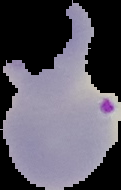

Cell region segmented out of the field of view; the surrounding area is masked to black. Result: malaria parasites identified. Image is 121×190 pixels. From a thin blood film.